Name the blood parasite species.
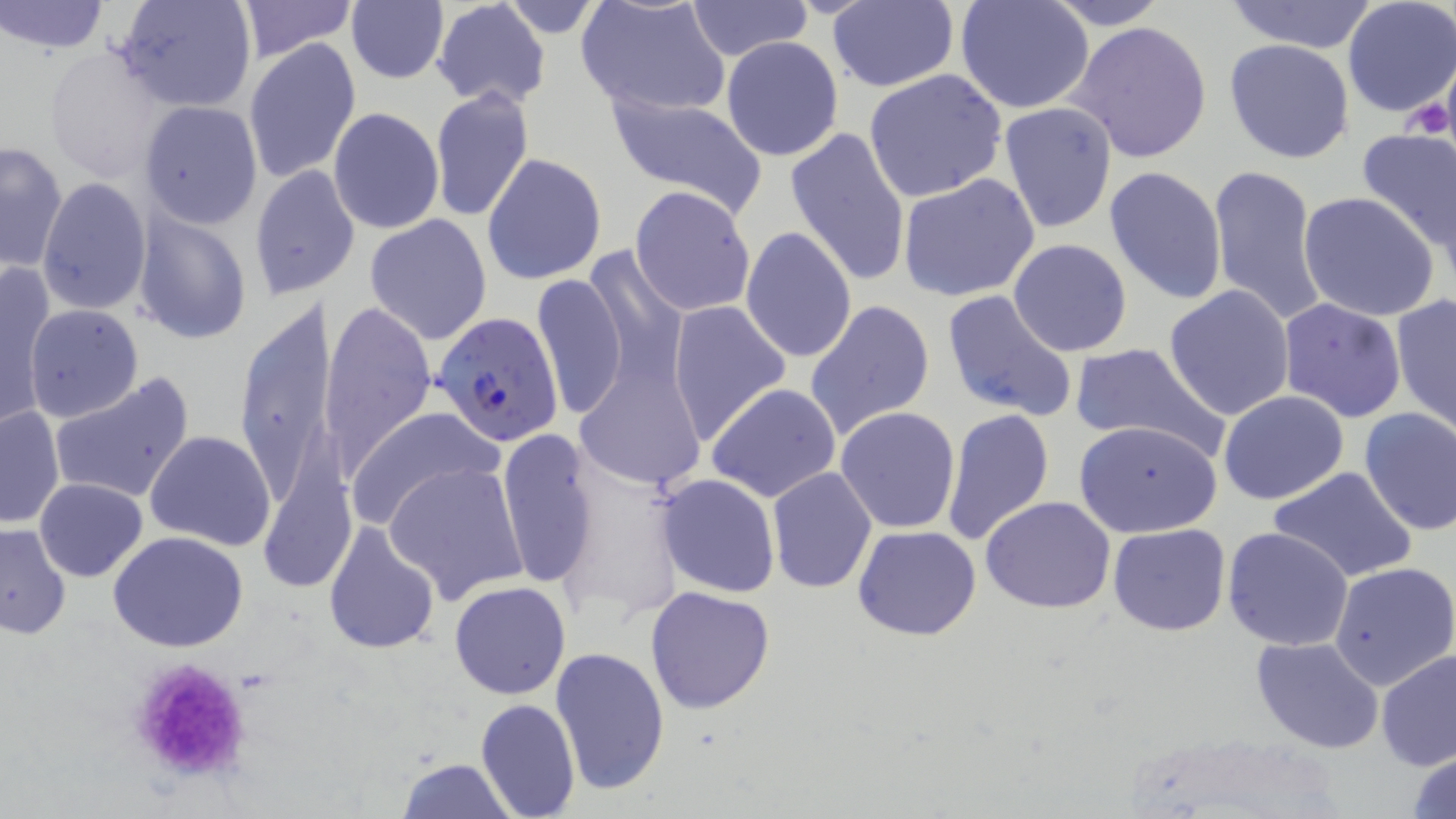
Plasmodium falciparum.

uninfected red blood cell locations = approximate bounding boxes as (x1, y1, x2, y2) in pixels: (1, 0, 112, 54), (112, 0, 258, 113), (235, 0, 360, 60), (685, 0, 813, 60), (955, 0, 1096, 113), (1045, 0, 1169, 29), (1220, 0, 1382, 52), (1342, 0, 1456, 118), (345, 1, 448, 85), (430, 1, 552, 111), (500, 1, 604, 36), (576, 1, 731, 120), (825, 1, 959, 91), (1066, 19, 1213, 162), (721, 36, 844, 162), (242, 37, 360, 185), (1224, 39, 1356, 164), (44, 46, 174, 183), (862, 68, 1006, 202), (429, 87, 534, 223), (602, 92, 766, 213), (138, 100, 263, 229), (998, 102, 1118, 234), (328, 107, 444, 235), (785, 125, 912, 287), (1355, 129, 1456, 254), (1, 140, 69, 273), (481, 153, 606, 287), (1207, 164, 1329, 329), (1102, 165, 1229, 306), (250, 166, 357, 299), (897, 173, 1041, 303), (37, 178, 151, 315), (629, 185, 756, 318), (1298, 191, 1442, 322), (131, 211, 253, 346), (364, 214, 493, 344), (740, 225, 857, 364), (1008, 238, 1133, 357), (581, 251, 690, 399), (0, 262, 56, 428), (532, 271, 629, 417), (1163, 284, 1296, 420), (230, 288, 344, 528), (940, 290, 1077, 424), (1390, 294, 1455, 435), (1276, 297, 1408, 423), (803, 299, 936, 439), (320, 301, 437, 477), (667, 302, 790, 443), (23, 304, 144, 423), (1068, 341, 1225, 455), (575, 362, 705, 496), (48, 372, 196, 505), (706, 381, 843, 502), (1218, 391, 1349, 507), (0, 405, 65, 529), (835, 406, 962, 534), (1358, 406, 1456, 535), (349, 408, 500, 528), (939, 408, 1053, 548), (1074, 419, 1224, 537), (497, 429, 601, 592), (144, 431, 276, 551), (386, 462, 529, 606), (766, 467, 878, 593), (1269, 467, 1417, 583), (655, 474, 782, 597), (35, 478, 149, 582), (979, 495, 1117, 613), (322, 520, 442, 656), (0, 524, 71, 638), (852, 524, 982, 641), (1107, 524, 1231, 637), (1222, 526, 1353, 651), (107, 530, 249, 653), (1328, 561, 1456, 689), (448, 581, 571, 700), (646, 585, 777, 715), (1250, 636, 1386, 754), (549, 647, 672, 797), (1377, 650, 1456, 773), (474, 698, 581, 819), (1406, 743, 1456, 819), (394, 756, 517, 818)
platelet locations = approximate bounding boxes as (x1, y1, x2, y2) in pixels: (1403, 95, 1452, 140), (122, 654, 260, 786)
magnification = 1000x
field of view = single
modality = optical microscopy
preparation = thin blood film
stain = May-Grünwald-Giemsa
image size = 1456×819 pixels
Plasmodium falciparum-infected red blood cell locations = approximate bounding boxes as (x1, y1, x2, y2) in pixels: (432, 313, 565, 446)